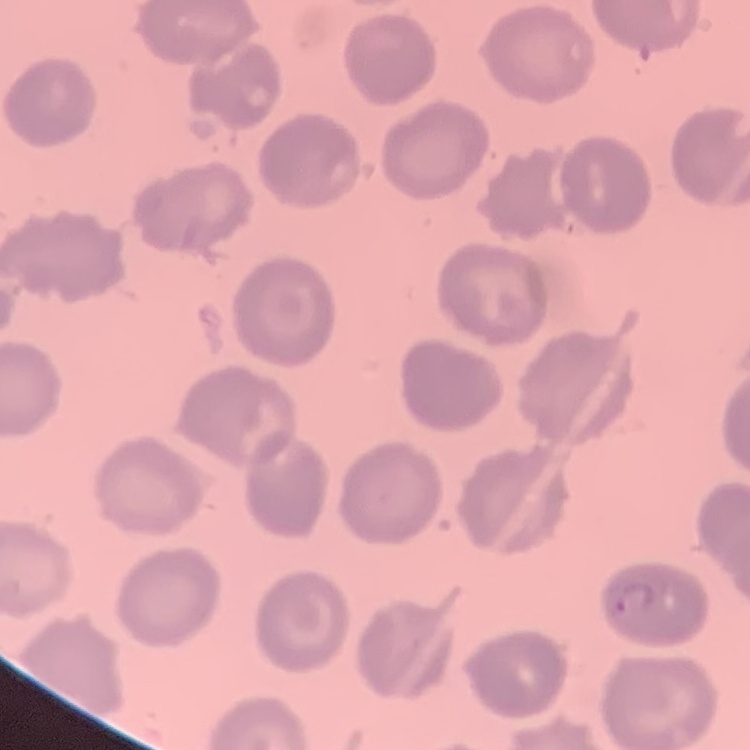
The erythrocytes show no rouleaux formation. Field's or Giemsa stain. Square crop of a larger photomicrograph. Thin peripheral smear.